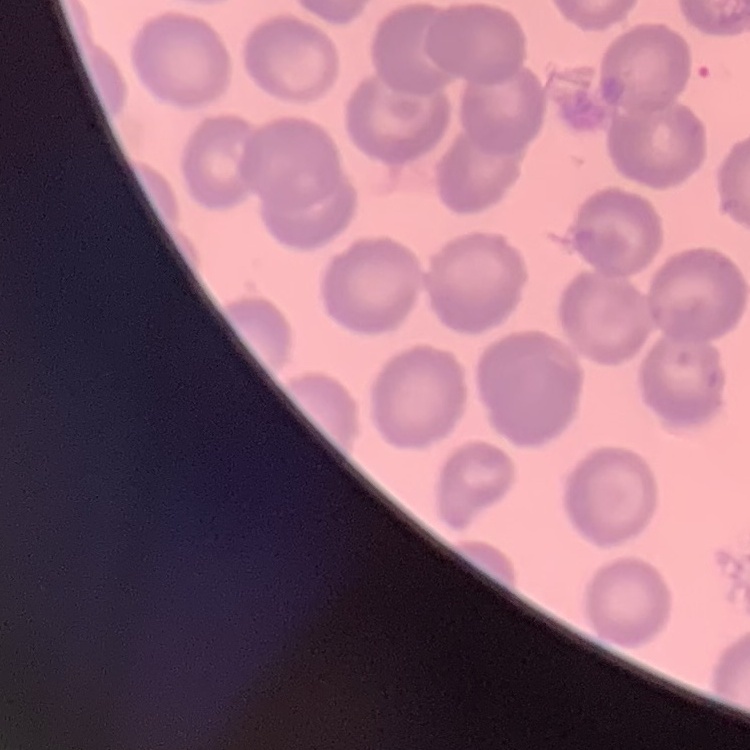 The erythrocytes exhibit no rouleaux formation. One tile cut from a larger photomicrograph. Thin blood film. Stained with either Field's or Giemsa.